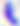 Photomicrograph. Captured at 400x magnification. Toxoplasma gondii is shown.